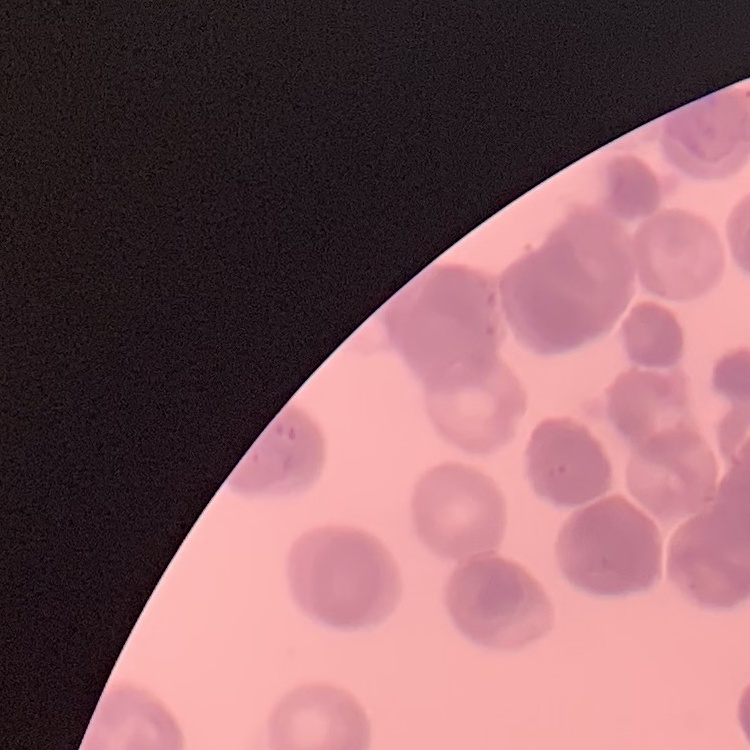
Summary:
  - Erythrocyte morphology: rouleaux formation
  - Stain: Field's or Giemsa
  - Preparation: thin blood smear
  - Image type: one tile cut from a larger photomicrograph